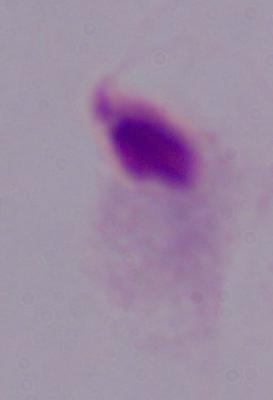 Captured at 1000x magnification. A trichomonad is seen. Micrograph.